Point out each Plasmodium parasite.
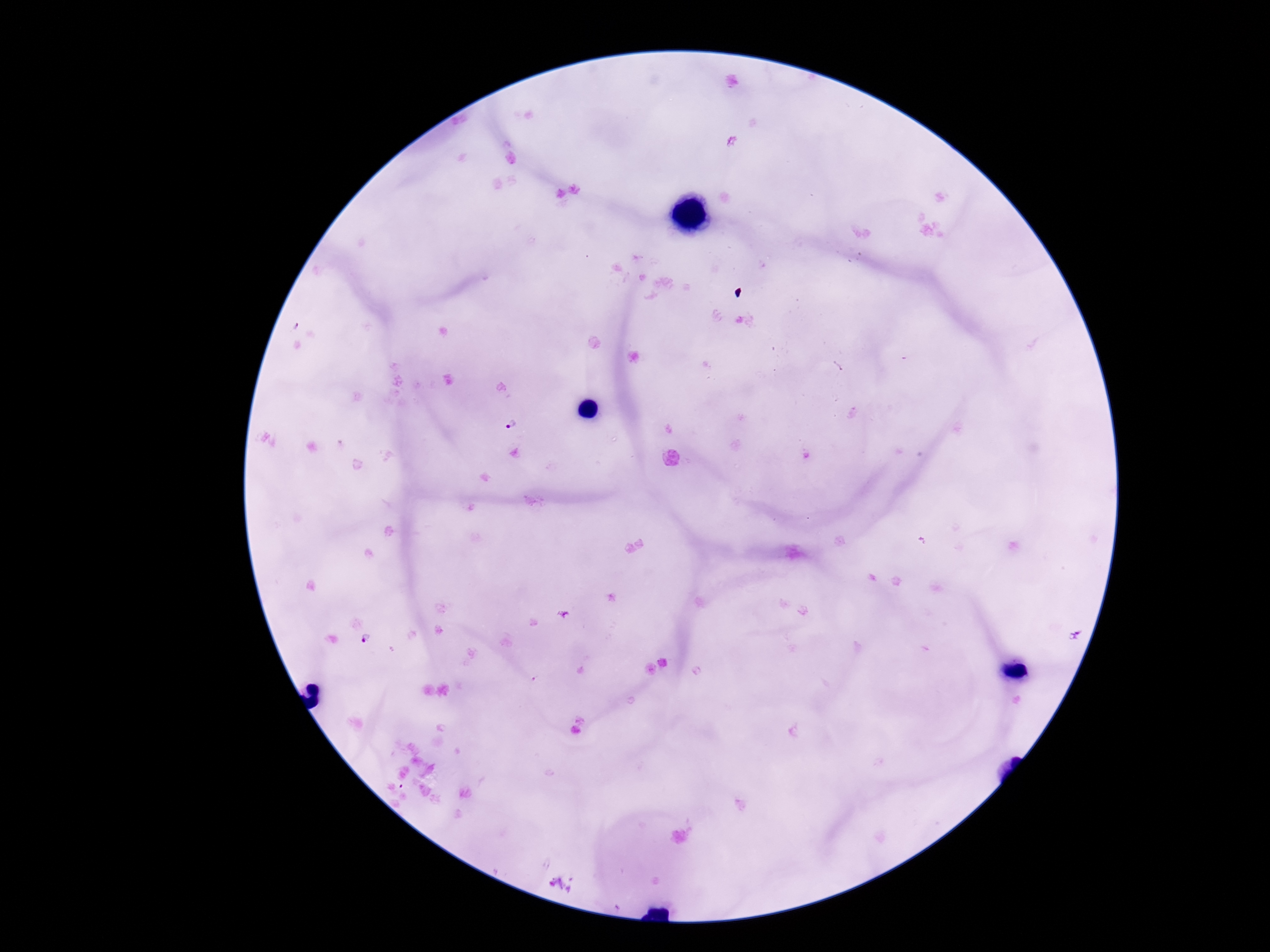

Approximate centers as (x, y) in pixels.
Plasmodium parasites: (512, 423).

image size = 1270×952 pixels
capture = smartphone camera through the microscope eyepiece
patient malaria status = positive
stain = Giemsa
preparation = thick blood smear
magnification = 100x
field of view = one from this slide